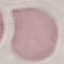

malaria status = uninfected
image type = cell patch, automatically extracted from a larger field of view and resized to 64 × 64 pixels
stain = Giemsa
capture = smartphone camera at the microscope eyepiece
preparation = thin blood smear